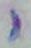 Toxoplasma gondii is shown. Photomicrograph. Captured at 1000x magnification.